State which cell type is depicted.
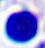

This is a leukocyte.

modality = micrograph
magnification = 400x